Report the malaria status of this cell.
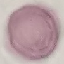

Uninfected.

Summary:
  - Capture: smartphone through the microscope eyepiece
  - Image type: cell patch, automatically extracted from a larger field of view and resized to 64 × 64 pixels
  - Preparation: thin blood smear
  - Stain: Giemsa